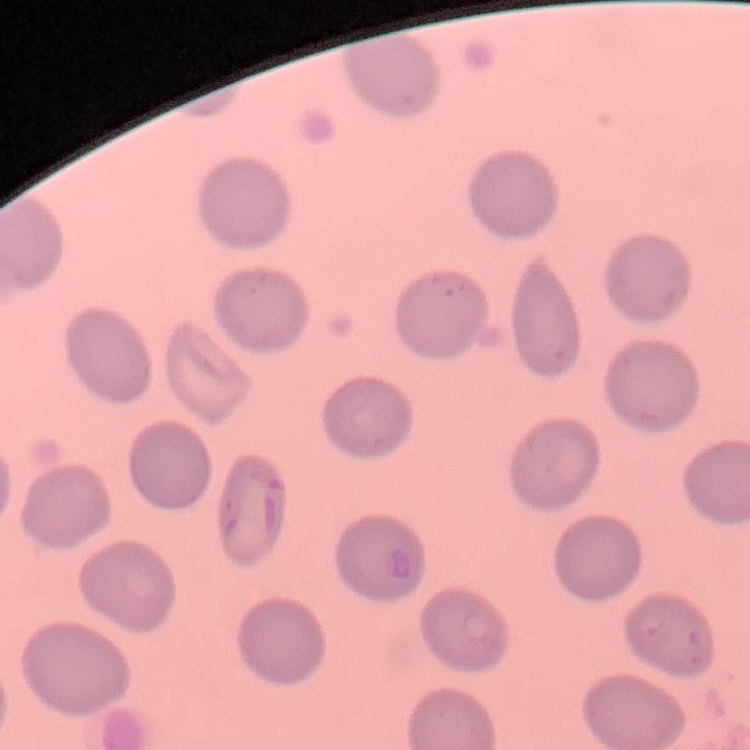

Summary:
  - Erythrocyte morphology: no rouleaux formation
  - Stain: Field's or Giemsa
  - Image type: one tile cut from a larger photomicrograph
  - Preparation: thin blood smear